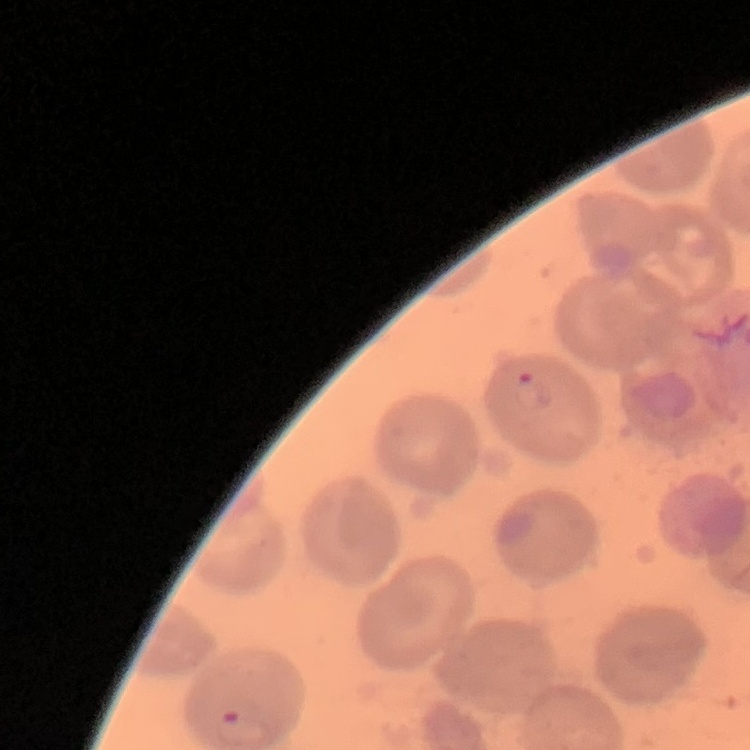
Summary:
  - Erythrocyte morphology: no rouleaux formation
  - Image type: square crop of a larger photomicrograph
  - Stain: Field's or Giemsa
  - Preparation: thin blood smear